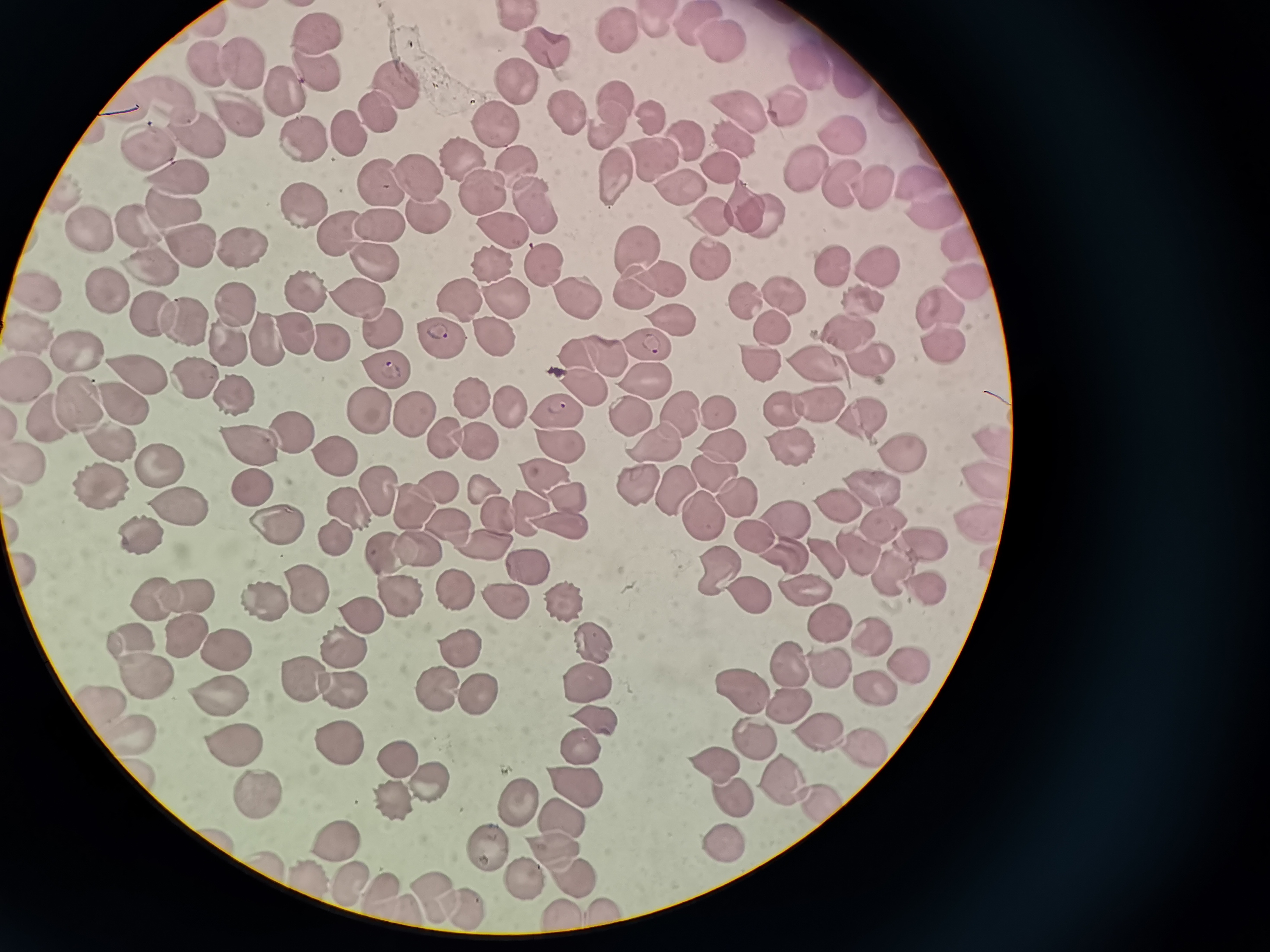
Approximate centers as (x, y) in pixels.
Summary:
  - Cell locations: (517, 17), (654, 22), (692, 24), (617, 28), (319, 32), (720, 37), (542, 50), (240, 58), (210, 66), (805, 70), (321, 76), (515, 77), (845, 81), (398, 84), (285, 91), (170, 96), (615, 99), (789, 103), (125, 104), (737, 109), (233, 112), (570, 113), (647, 115), (498, 117), (374, 118), (604, 125), (349, 133), (847, 136), (683, 137), (307, 138), (731, 138), (197, 139), (147, 148), (468, 153), (650, 157), (719, 164), (804, 164), (522, 169), (610, 169), (416, 173), (182, 179), (915, 180), (875, 182), (376, 185), (840, 185), (678, 187), (487, 196), (744, 199), (304, 200), (535, 203), (933, 203), (172, 206), (762, 208), (426, 212), (710, 212), (88, 224), (377, 225), (138, 227), (341, 231), (503, 232), (955, 235), (242, 241), (190, 246), (640, 247), (368, 259), (491, 261), (837, 261), (143, 264), (711, 264), (543, 265), (878, 265), (657, 278), (964, 281), (630, 283), (304, 291), (782, 292), (106, 293), (457, 293), (861, 295), (41, 296), (572, 296), (357, 297), (505, 297), (753, 298), (235, 303), (936, 305), (152, 312), (676, 314), (773, 321), (182, 322), (384, 328), (852, 329), (297, 331), (321, 334), (490, 334), (34, 335), (441, 335), (265, 338), (943, 340), (227, 342), (654, 342), (605, 354), (871, 356), (78, 357), (579, 357), (760, 358), (822, 362), (388, 366), (138, 369), (30, 376), (648, 376), (192, 380), (579, 383), (229, 390), (468, 397), (75, 400), (819, 400), (117, 401), (510, 406), (561, 408), (715, 408), (785, 408), (368, 412), (411, 412), (627, 412), (679, 413), (863, 415), (48, 416), (290, 432), (443, 435), (99, 438), (786, 438), (475, 439), (557, 439), (655, 441), (251, 442), (723, 442), (990, 442), (897, 447), (333, 453), (29, 460), (159, 465), (710, 469), (543, 478), (673, 480), (985, 481), (635, 482), (103, 485), (250, 485), (871, 485), (480, 487), (438, 489), (378, 495), (734, 498), (570, 499), (412, 501), (831, 503), (176, 509), (698, 509), (529, 510), (348, 512), (493, 516), (781, 518), (979, 519), (878, 521), (274, 524), (446, 525), (558, 527), (756, 531), (140, 534), (924, 538), (333, 541), (478, 544), (419, 546), (825, 550), (858, 552), (786, 554), (389, 555), (717, 563), (530, 568), (892, 570), (452, 586), (304, 587), (925, 587), (796, 588), (395, 589), (185, 592), (743, 593), (152, 596), (266, 599), (565, 599), (507, 604), (362, 615), (828, 621), (180, 633), (871, 635), (131, 636), (342, 641), (594, 643), (228, 646), (457, 646), (791, 663), (823, 663), (904, 663), (141, 677), (303, 677), (740, 677), (870, 678), (584, 682), (433, 686), (346, 688), (480, 693), (219, 697), (97, 701), (788, 705), (596, 718), (822, 731), (754, 735), (128, 736), (230, 742), (336, 743), (580, 743), (861, 745), (717, 761), (395, 763), (569, 778), (780, 779), (427, 782), (252, 787), (728, 794), (514, 797), (814, 797), (396, 807), (564, 819), (720, 836), (341, 843), (556, 849), (490, 852), (270, 864), (577, 875), (309, 877), (528, 880), (351, 883), (384, 889), (435, 894), (464, 905), (400, 909), (607, 909), (562, 914)
  - Preparation: thin smear
  - Stain: Giemsa
  - Field of view: single
  - Image size: 1270×952 pixels
  - Capture: smartphone through the microscope eyepiece